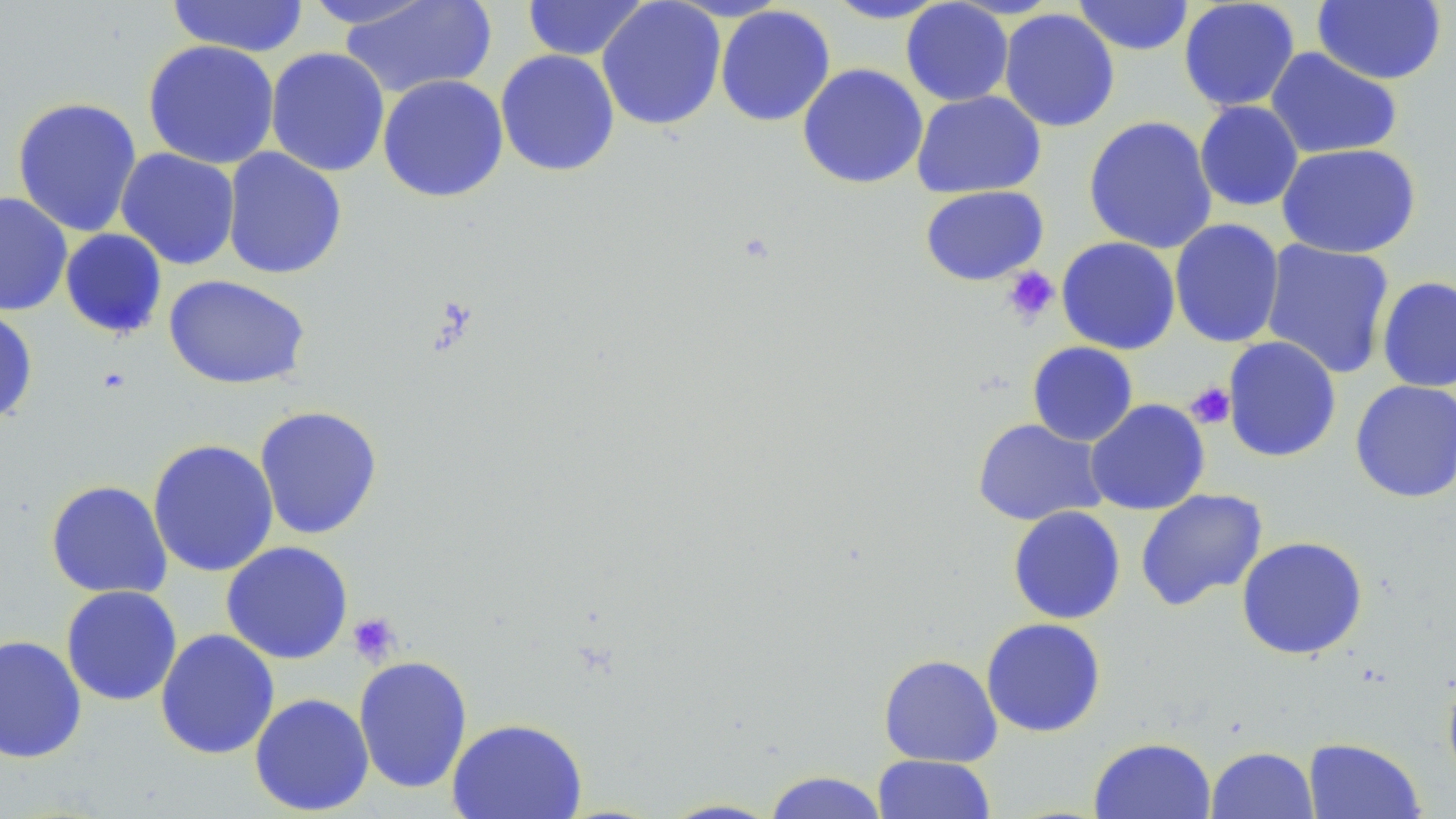

slide-level diagnosis = negative for blood parasites
stain = May-Grünwald-Giemsa
platelet locations = approximate bounding boxes as named x1/y1/x2/y2 corners in pixels: (x1=1001, y1=267, x2=1059, y2=326), (x1=1186, y1=383, x2=1235, y2=429), (x1=347, y1=611, x2=401, y2=664)
uninfected red blood cell locations = approximate bounding boxes as named x1/y1/x2/y2 corners in pixels: (x1=166, y1=0, x2=310, y2=58), (x1=338, y1=0, x2=498, y2=99), (x1=597, y1=0, x2=727, y2=131), (x1=821, y1=0, x2=954, y2=24), (x1=1072, y1=0, x2=1195, y2=56), (x1=1178, y1=0, x2=1300, y2=112), (x1=1312, y1=0, x2=1447, y2=85), (x1=299, y1=1, x2=441, y2=30), (x1=521, y1=1, x2=652, y2=61), (x1=900, y1=1, x2=1014, y2=106), (x1=714, y1=5, x2=836, y2=127), (x1=998, y1=8, x2=1120, y2=132), (x1=142, y1=39, x2=281, y2=170), (x1=265, y1=47, x2=390, y2=177), (x1=1265, y1=47, x2=1403, y2=160), (x1=495, y1=49, x2=620, y2=177), (x1=797, y1=63, x2=929, y2=189), (x1=377, y1=74, x2=509, y2=203), (x1=911, y1=90, x2=1046, y2=198), (x1=11, y1=96, x2=143, y2=238), (x1=1194, y1=100, x2=1304, y2=212), (x1=1083, y1=115, x2=1218, y2=255), (x1=1277, y1=143, x2=1422, y2=259), (x1=222, y1=147, x2=347, y2=280), (x1=115, y1=148, x2=240, y2=270), (x1=919, y1=185, x2=1049, y2=286), (x1=0, y1=191, x2=73, y2=317), (x1=1169, y1=218, x2=1285, y2=349), (x1=59, y1=228, x2=168, y2=340), (x1=1056, y1=236, x2=1181, y2=355), (x1=1260, y1=239, x2=1396, y2=379), (x1=163, y1=274, x2=311, y2=390), (x1=1377, y1=276, x2=1456, y2=393), (x1=0, y1=307, x2=39, y2=425), (x1=1222, y1=336, x2=1342, y2=463), (x1=1026, y1=341, x2=1139, y2=446), (x1=1350, y1=380, x2=1456, y2=503), (x1=1085, y1=399, x2=1211, y2=516), (x1=254, y1=405, x2=383, y2=540), (x1=972, y1=418, x2=1107, y2=526), (x1=147, y1=438, x2=279, y2=578), (x1=45, y1=479, x2=173, y2=599), (x1=1135, y1=488, x2=1268, y2=611), (x1=1007, y1=505, x2=1126, y2=625), (x1=1236, y1=535, x2=1369, y2=660), (x1=220, y1=541, x2=354, y2=664), (x1=60, y1=585, x2=182, y2=706), (x1=981, y1=617, x2=1107, y2=738), (x1=155, y1=629, x2=280, y2=760), (x1=0, y1=634, x2=87, y2=764), (x1=878, y1=654, x2=1003, y2=767), (x1=352, y1=655, x2=473, y2=794), (x1=1441, y1=670, x2=1456, y2=788), (x1=249, y1=692, x2=374, y2=816), (x1=446, y1=716, x2=588, y2=818), (x1=1088, y1=736, x2=1216, y2=818), (x1=1303, y1=737, x2=1426, y2=819), (x1=1206, y1=746, x2=1318, y2=819), (x1=872, y1=754, x2=996, y2=818), (x1=761, y1=770, x2=890, y2=819), (x1=655, y1=797, x2=785, y2=818)
field of view = single
magnification = 1000x
modality = optical microscopy
preparation = thin blood film
image size = 1456×819 pixels